Outline each Plasmodium vivax-infected red blood cell.
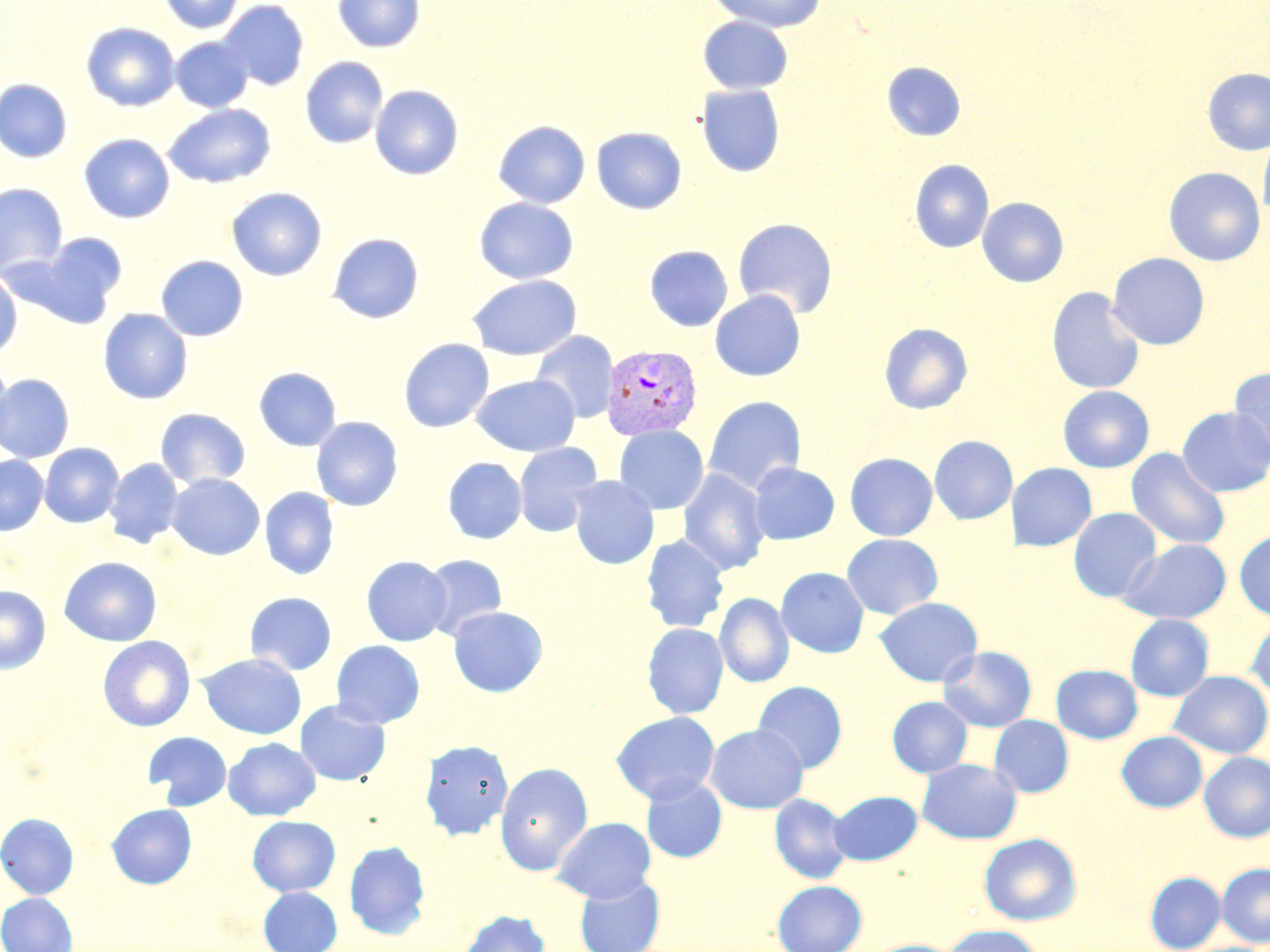

Approximate bounding boxes as named x1/y1/x2/y2 corners in pixels.
Plasmodium vivax-infected red blood cells: (x1=600, y1=344, x2=703, y2=441).

slide-level diagnosis = Plasmodium vivax
image size = 1270×952 pixels
stain = May-Grünwald-Giemsa
preparation = thin blood film
uninfected red blood cell locations = approximate bounding boxes as named x1/y1/x2/y2 corners in pixels: (x1=159, y1=0, x2=244, y2=34), (x1=218, y1=0, x2=309, y2=90), (x1=333, y1=0, x2=424, y2=53), (x1=707, y1=0, x2=828, y2=32), (x1=698, y1=16, x2=793, y2=94), (x1=81, y1=22, x2=180, y2=112), (x1=171, y1=36, x2=254, y2=112), (x1=301, y1=57, x2=388, y2=148), (x1=882, y1=61, x2=966, y2=141), (x1=1202, y1=67, x2=1270, y2=156), (x1=0, y1=78, x2=73, y2=163), (x1=370, y1=84, x2=464, y2=180), (x1=696, y1=84, x2=785, y2=177), (x1=163, y1=104, x2=276, y2=188), (x1=493, y1=120, x2=591, y2=208), (x1=591, y1=127, x2=687, y2=215), (x1=1258, y1=130, x2=1270, y2=224), (x1=80, y1=133, x2=174, y2=223), (x1=909, y1=159, x2=995, y2=253), (x1=1163, y1=167, x2=1265, y2=266), (x1=0, y1=183, x2=67, y2=276), (x1=227, y1=187, x2=327, y2=280), (x1=474, y1=197, x2=578, y2=284), (x1=977, y1=197, x2=1069, y2=288), (x1=733, y1=218, x2=838, y2=319), (x1=28, y1=233, x2=127, y2=327), (x1=327, y1=233, x2=424, y2=324), (x1=645, y1=246, x2=733, y2=332), (x1=1107, y1=252, x2=1210, y2=350), (x1=155, y1=255, x2=248, y2=342), (x1=0, y1=270, x2=22, y2=359), (x1=468, y1=275, x2=581, y2=360), (x1=1046, y1=287, x2=1146, y2=395), (x1=709, y1=290, x2=806, y2=381), (x1=98, y1=309, x2=193, y2=404), (x1=879, y1=322, x2=972, y2=414), (x1=531, y1=331, x2=619, y2=423), (x1=399, y1=338, x2=494, y2=432), (x1=0, y1=363, x2=15, y2=453), (x1=254, y1=366, x2=341, y2=451), (x1=1228, y1=366, x2=1270, y2=464), (x1=0, y1=374, x2=74, y2=462), (x1=471, y1=374, x2=580, y2=456), (x1=1057, y1=386, x2=1154, y2=472), (x1=703, y1=396, x2=806, y2=495), (x1=1178, y1=406, x2=1270, y2=497), (x1=155, y1=408, x2=251, y2=489), (x1=311, y1=416, x2=403, y2=512), (x1=613, y1=425, x2=709, y2=515), (x1=929, y1=435, x2=1018, y2=524), (x1=514, y1=442, x2=604, y2=537), (x1=40, y1=443, x2=123, y2=527), (x1=1126, y1=447, x2=1231, y2=550), (x1=844, y1=452, x2=938, y2=541), (x1=0, y1=455, x2=49, y2=535), (x1=443, y1=457, x2=527, y2=544), (x1=104, y1=458, x2=184, y2=549), (x1=1006, y1=462, x2=1096, y2=551), (x1=748, y1=463, x2=839, y2=544), (x1=678, y1=469, x2=770, y2=575), (x1=167, y1=473, x2=265, y2=560), (x1=568, y1=475, x2=659, y2=569), (x1=259, y1=487, x2=339, y2=580), (x1=1068, y1=507, x2=1162, y2=603), (x1=1234, y1=530, x2=1270, y2=621), (x1=641, y1=534, x2=729, y2=633), (x1=841, y1=534, x2=943, y2=619), (x1=1118, y1=539, x2=1232, y2=624), (x1=420, y1=554, x2=508, y2=639), (x1=58, y1=556, x2=163, y2=646), (x1=361, y1=556, x2=452, y2=646), (x1=776, y1=567, x2=869, y2=658), (x1=0, y1=586, x2=51, y2=674), (x1=244, y1=592, x2=337, y2=676), (x1=714, y1=593, x2=794, y2=688), (x1=873, y1=597, x2=983, y2=687), (x1=448, y1=606, x2=547, y2=697), (x1=1125, y1=614, x2=1214, y2=702), (x1=1247, y1=616, x2=1270, y2=698), (x1=642, y1=622, x2=729, y2=719), (x1=97, y1=636, x2=195, y2=732), (x1=330, y1=640, x2=425, y2=729), (x1=938, y1=646, x2=1037, y2=733), (x1=197, y1=653, x2=307, y2=740), (x1=1051, y1=664, x2=1143, y2=743), (x1=1169, y1=671, x2=1270, y2=759), (x1=752, y1=681, x2=847, y2=773), (x1=887, y1=696, x2=973, y2=778), (x1=294, y1=699, x2=391, y2=787), (x1=611, y1=711, x2=720, y2=805), (x1=989, y1=715, x2=1073, y2=798), (x1=706, y1=724, x2=808, y2=813), (x1=143, y1=731, x2=233, y2=811), (x1=1117, y1=731, x2=1207, y2=813), (x1=223, y1=738, x2=321, y2=821), (x1=419, y1=739, x2=514, y2=841), (x1=1199, y1=752, x2=1270, y2=842), (x1=916, y1=758, x2=1022, y2=844), (x1=495, y1=762, x2=592, y2=875), (x1=641, y1=775, x2=727, y2=862), (x1=828, y1=790, x2=923, y2=865), (x1=768, y1=794, x2=852, y2=884), (x1=106, y1=803, x2=197, y2=889), (x1=0, y1=813, x2=79, y2=899), (x1=247, y1=815, x2=340, y2=896), (x1=552, y1=816, x2=656, y2=902), (x1=978, y1=832, x2=1081, y2=926), (x1=344, y1=840, x2=430, y2=940), (x1=1217, y1=863, x2=1270, y2=947), (x1=1145, y1=871, x2=1225, y2=951), (x1=574, y1=874, x2=665, y2=952), (x1=772, y1=880, x2=867, y2=952), (x1=258, y1=886, x2=342, y2=952), (x1=0, y1=892, x2=78, y2=952), (x1=458, y1=910, x2=550, y2=952), (x1=941, y1=926, x2=1046, y2=952), (x1=863, y1=939, x2=965, y2=952)
field of view = single
modality = optical microscopy
magnification = 1000x